Give the extent of all uninfected red blood cells.
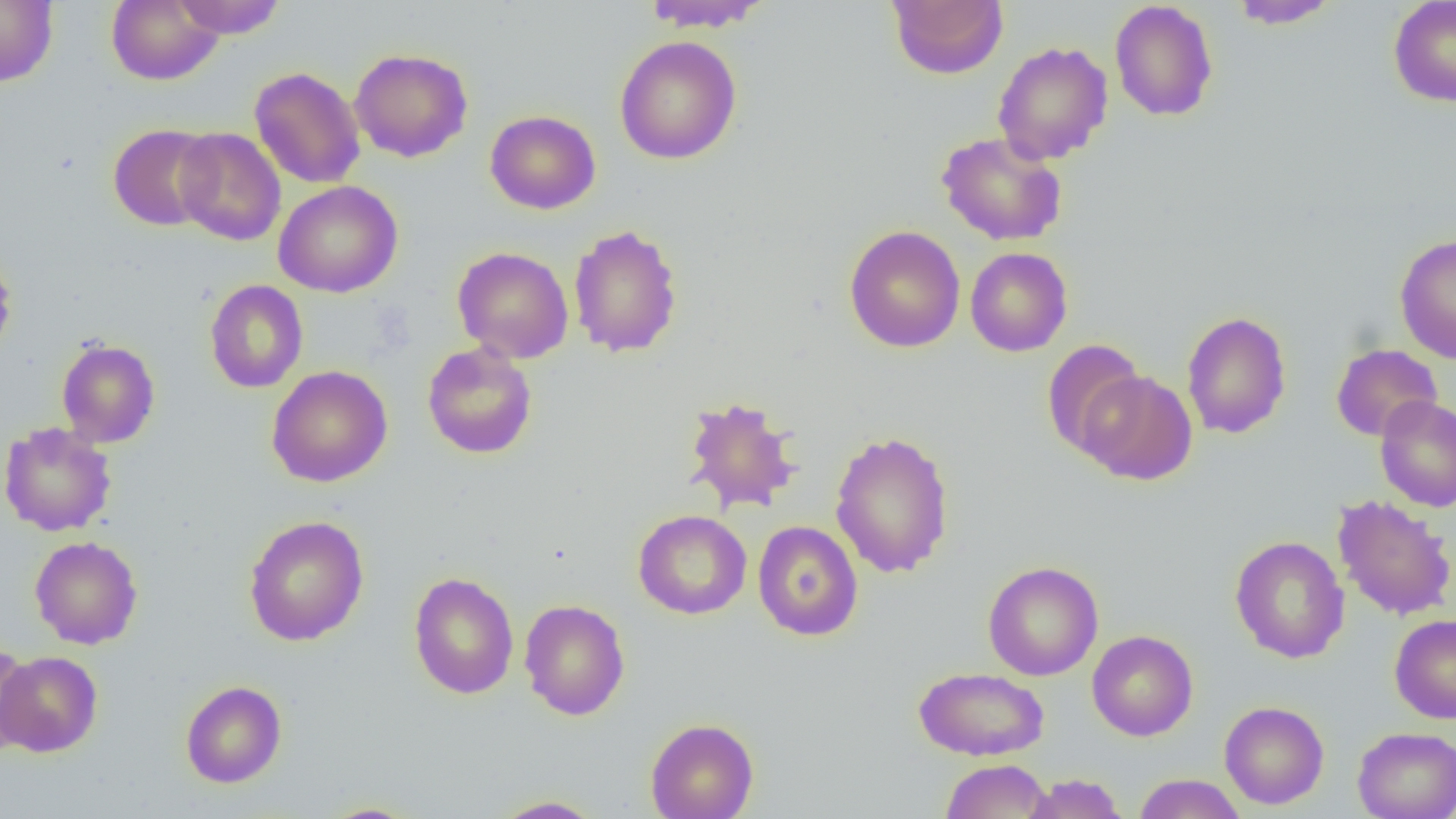

Approximate bounding boxes as (x1, y1, x2, y2) in pixels.
Uninfected red blood cells: (106, 0, 223, 86), (171, 0, 288, 38), (641, 0, 774, 32), (887, 0, 1008, 80), (1228, 0, 1341, 29), (1388, 0, 1456, 107), (0, 1, 58, 87), (1109, 1, 1219, 122), (614, 35, 742, 165), (992, 40, 1113, 165), (349, 47, 474, 162), (249, 67, 365, 188), (485, 110, 600, 214), (108, 124, 219, 231), (174, 127, 285, 246), (936, 131, 1068, 246), (274, 180, 402, 298), (568, 224, 684, 359), (844, 225, 965, 353), (1394, 233, 1456, 363), (451, 246, 574, 363), (964, 247, 1073, 356), (0, 248, 17, 362), (204, 280, 308, 393), (1181, 310, 1292, 439), (56, 338, 160, 448), (1041, 339, 1148, 460), (422, 342, 538, 459), (1331, 344, 1443, 441), (266, 365, 393, 488), (1077, 369, 1198, 485), (682, 395, 803, 515), (1375, 395, 1456, 512), (0, 422, 117, 537), (830, 430, 955, 579), (1332, 494, 1456, 621), (633, 509, 752, 619), (244, 515, 369, 646), (752, 520, 863, 641), (29, 535, 143, 649), (1229, 535, 1349, 663), (982, 560, 1104, 680), (408, 571, 520, 699), (519, 598, 631, 721), (1389, 613, 1456, 724), (1087, 630, 1198, 741), (0, 645, 37, 754), (0, 651, 103, 757), (913, 666, 1050, 761), (180, 680, 287, 787), (1219, 700, 1329, 809), (645, 717, 759, 819), (1352, 727, 1456, 819), (939, 759, 1053, 818), (1022, 773, 1129, 819), (1133, 773, 1246, 818), (488, 795, 606, 818), (317, 802, 424, 819).

slide-level diagnosis = no evidence of blood parasites
modality = optical microscopy
image size = 1456×819 pixels
preparation = thin blood film
magnification = 1000x
field of view = one of a larger specimen